Point out each leukocyte.
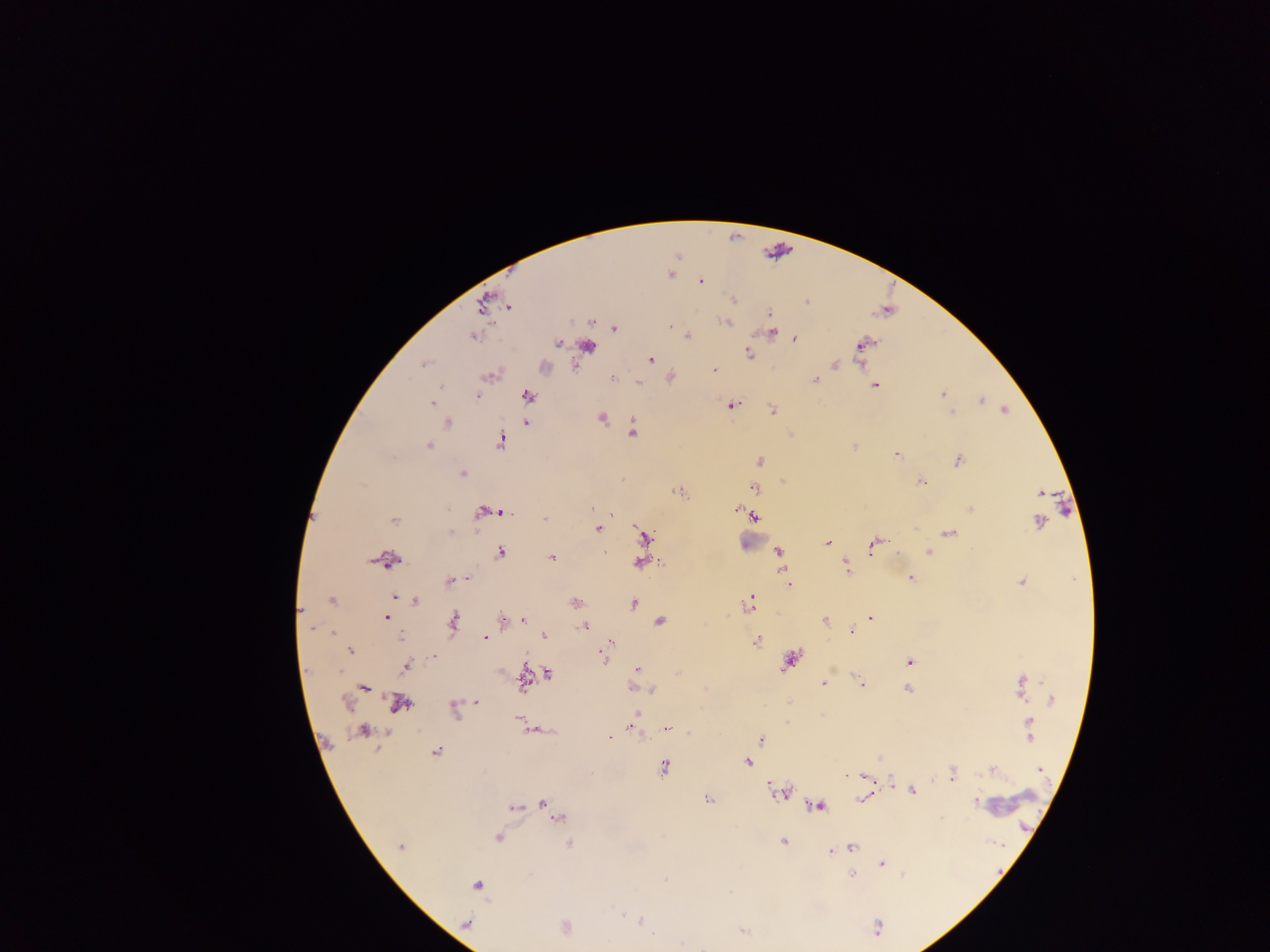
Approximate centers as [x, y] in pixels.
Leukocytes: [592, 346], [546, 367], [750, 538], [1013, 801].

{
  "image_size": "1270×952 pixels",
  "country": "Ghana",
  "preparation": "thick blood film",
  "malaria_parasite_locations": "approximate centers as [x, y] in pixels: [670, 274], [700, 281], [733, 300], [806, 303], [508, 306], [769, 313], [724, 322], [669, 325], [615, 328], [772, 332], [472, 336], [687, 336], [794, 340], [559, 342], [865, 343], [748, 353], [651, 359], [424, 364], [835, 365], [714, 370], [490, 375], [671, 377], [613, 378], [815, 380], [639, 382], [875, 386], [942, 394], [477, 397], [528, 397], [981, 400], [431, 404], [732, 406], [1005, 410], [772, 411], [951, 412], [602, 418], [447, 423], [526, 423], [633, 430], [500, 441], [429, 445], [854, 446], [896, 454], [760, 461], [958, 461], [462, 474], [920, 482], [755, 488], [679, 492], [1040, 492], [738, 509], [971, 509], [482, 512], [501, 512], [612, 516], [753, 516], [545, 518], [394, 521], [1038, 522], [599, 529], [451, 532], [950, 532], [646, 537], [827, 543], [873, 544], [779, 551], [928, 552], [501, 553], [606, 554], [551, 557], [389, 561], [640, 562], [847, 567], [911, 577], [785, 578], [464, 579], [450, 580], [1022, 582], [789, 584], [395, 597], [332, 601], [415, 602], [750, 602], [574, 603], [634, 604], [300, 611], [386, 617], [871, 617], [503, 619], [523, 619], [825, 620], [660, 621], [453, 622], [584, 626], [851, 632], [543, 636], [399, 637], [485, 637], [756, 642], [609, 646], [350, 650], [433, 656], [603, 657], [789, 661], [909, 661], [406, 667], [638, 668], [548, 673], [677, 673], [823, 684], [860, 684], [1021, 685], [632, 687], [364, 688], [908, 689], [652, 690], [1052, 698], [476, 702], [789, 702], [343, 703], [400, 704], [455, 710], [637, 713], [519, 718], [632, 728], [1028, 728], [666, 729], [363, 731], [609, 736], [761, 739], [435, 752], [748, 762], [665, 768], [1039, 769], [992, 771], [952, 774], [865, 776], [912, 791], [779, 792], [863, 799], [707, 800], [977, 802], [544, 805], [818, 806], [515, 807], [557, 816], [497, 838], [783, 841], [569, 843], [399, 846], [852, 848], [831, 851], [881, 864], [852, 875], [477, 885], [640, 921], [565, 926], [876, 928], [742, 932]",
  "field_of_view": "single",
  "capture": "mobile-phone photograph through a microscope"
}